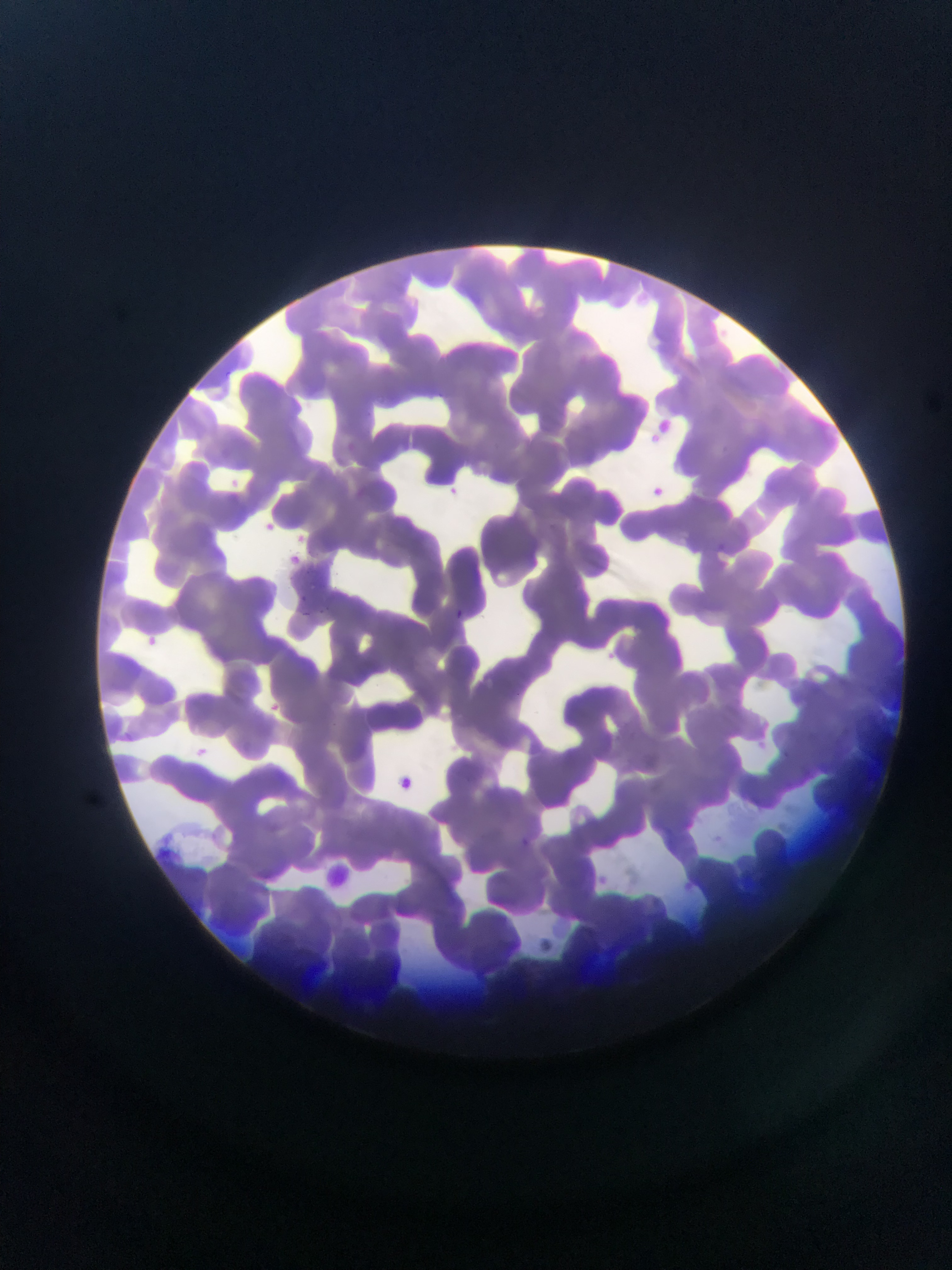
{
  "image_size": "952×1270 pixels",
  "country": "Ghana",
  "capture": "mobile-phone photograph through a microscope",
  "field_of_view": "single",
  "plasmodium_parasite_locations": "approximate bounding boxes as {left, top, right, bottom} in pixels: {223, 368, 234, 377}, {449, 485, 462, 500}, {255, 516, 280, 539}, {297, 594, 307, 603}, {322, 604, 335, 619}, {299, 609, 315, 618}, {451, 609, 467, 620}, {141, 633, 162, 651}, {187, 742, 214, 765}, {389, 774, 417, 798}, {523, 837, 534, 850}",
  "preparation": "thin blood smear",
  "leukocyte_locations": "approximate bounding boxes as {left, top, right, bottom} in pixels: {322, 860, 356, 890}"
}